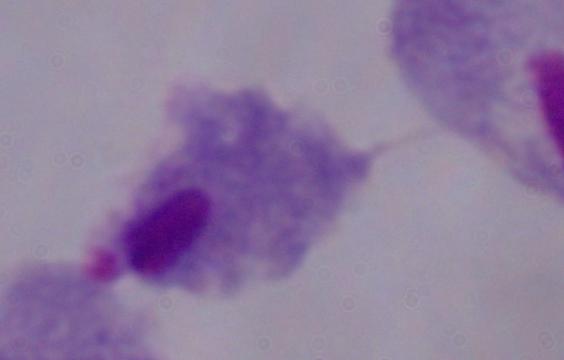
identification: trichomonad
modality: micrograph
magnification: 1000x